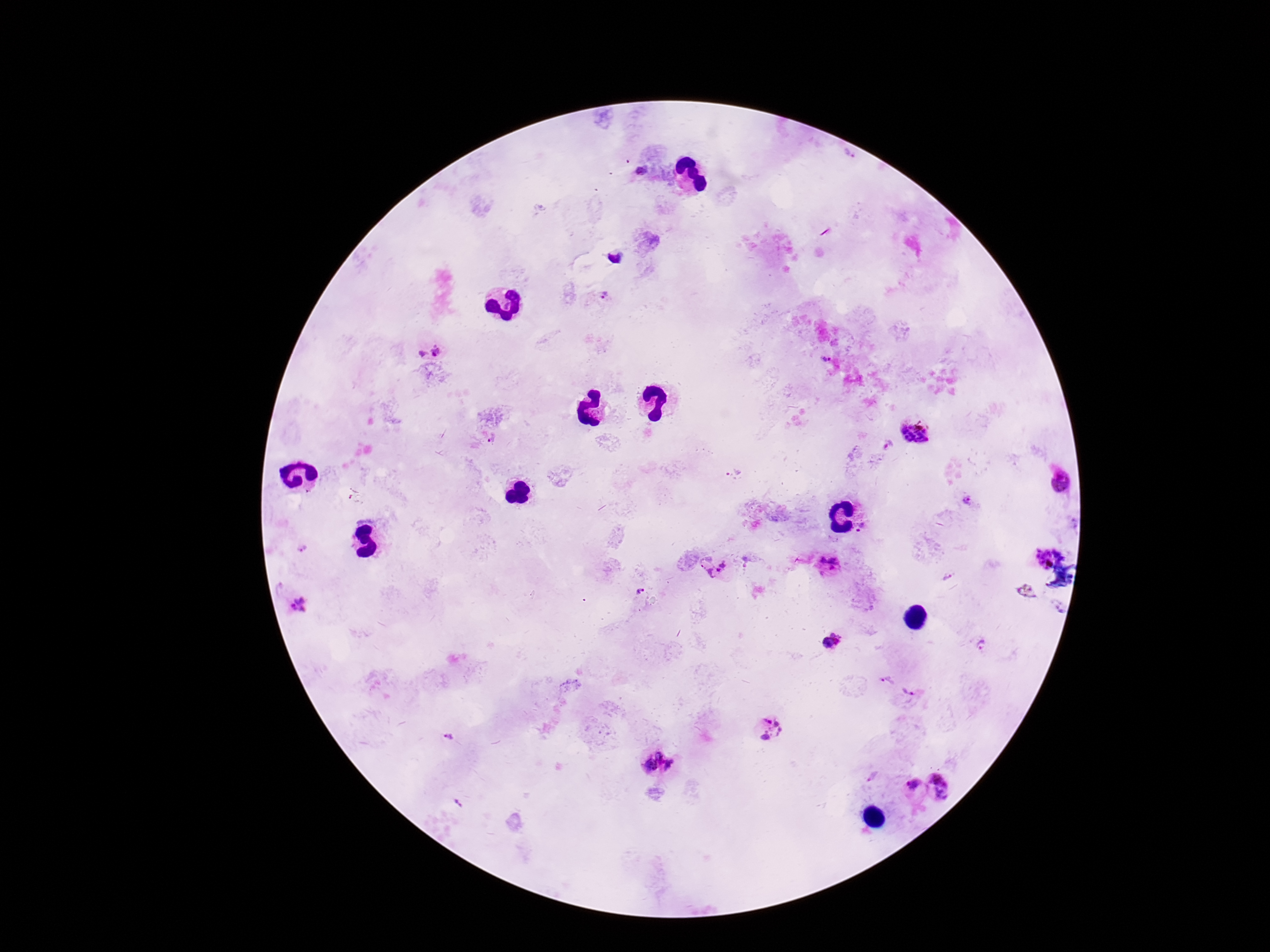

Approximate centers as [x, y] in pixels. Plasmodium parasite locations: [849, 153], [642, 170], [604, 296], [438, 352], [422, 354], [826, 359], [914, 431], [493, 439], [734, 474], [1060, 480], [969, 500], [862, 524], [858, 530], [302, 548], [1043, 558], [833, 559], [823, 560], [705, 561], [723, 564], [832, 569], [719, 570], [710, 574], [947, 578], [641, 591], [1027, 591], [298, 604], [1060, 607], [832, 635], [841, 641], [827, 643], [982, 646], [888, 681], [908, 690], [769, 729], [449, 738], [661, 756], [650, 765], [672, 765], [872, 777], [942, 785], [912, 787], [458, 804]. 100x magnification. Single field of view. Thick blood smear. Image is 1270×952 pixels. Photographed through the microscope eyepiece with a smartphone camera. Giemsa stain. Patient malaria status: infected.